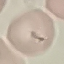
result: no malaria parasites detected
capture: smartphone camera at the microscope eyepiece
preparation: thin blood smear
stain: Giemsa
image_type: cell patch, automatically extracted from a larger field of view and resized to 64 × 64 pixels